Assess the morphology of the erythrocytes.
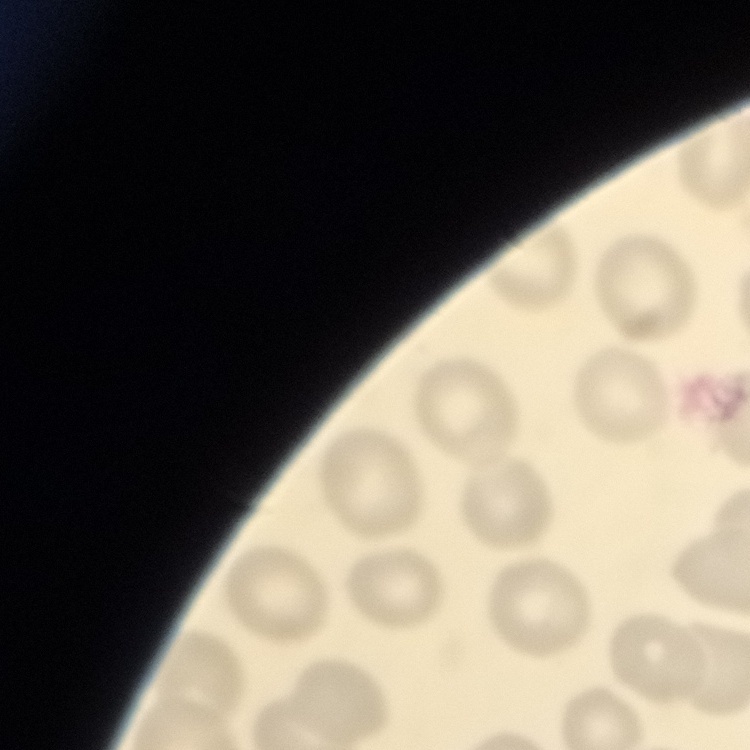

No rouleaux formation.

stain = Field's or Giemsa
preparation = thin blood film
image type = one tile cut from a larger photomicrograph